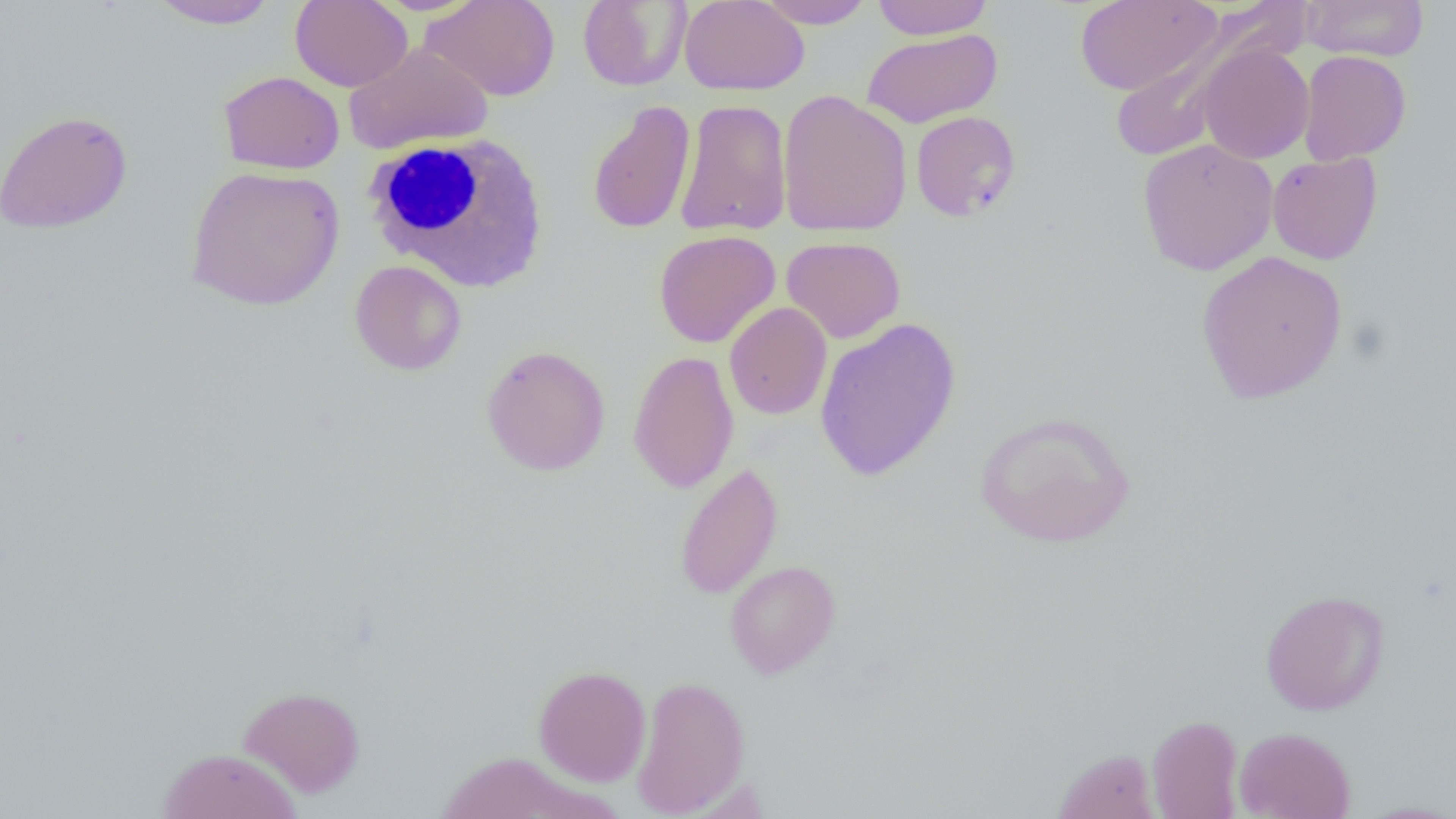

slide-level diagnosis = no evidence of blood parasites
field of view = one of a larger specimen
magnification = 1000x
uninfected red blood cell locations = approximate bounding boxes as (x1, y1, x2, y2) in pixels: (290, 0, 413, 91), (420, 0, 560, 101), (872, 0, 994, 39), (1075, 0, 1222, 95), (1299, 0, 1429, 61), (149, 1, 280, 30), (577, 1, 691, 91), (679, 1, 809, 96), (754, 1, 876, 29), (1114, 26, 1262, 162), (860, 28, 1003, 128), (343, 41, 494, 155), (1196, 43, 1315, 164), (1298, 50, 1411, 165), (218, 71, 345, 174), (777, 90, 912, 237), (675, 99, 793, 237), (587, 100, 696, 235), (0, 109, 132, 234), (910, 110, 1021, 222), (1137, 138, 1278, 276), (1267, 152, 1382, 265), (185, 166, 344, 311), (654, 230, 781, 348), (781, 236, 906, 343), (1196, 250, 1348, 404), (350, 260, 467, 375), (724, 302, 831, 420), (814, 317, 961, 482), (481, 344, 610, 476), (628, 349, 739, 494), (974, 410, 1137, 549), (674, 462, 783, 599), (724, 560, 841, 679), (1260, 588, 1390, 715), (533, 664, 651, 786), (631, 675, 750, 817), (238, 685, 366, 798), (1147, 714, 1244, 819), (1234, 726, 1357, 819), (1053, 747, 1160, 819), (158, 748, 302, 818), (434, 751, 594, 819), (1355, 800, 1456, 818)
modality = light microscopy
image size = 1456×819 pixels
preparation = thin blood film
white blood cell locations = approximate bounding boxes as (x1, y1, x2, y2) in pixels: (360, 132, 551, 293)